Give the extent of all white blood cells.
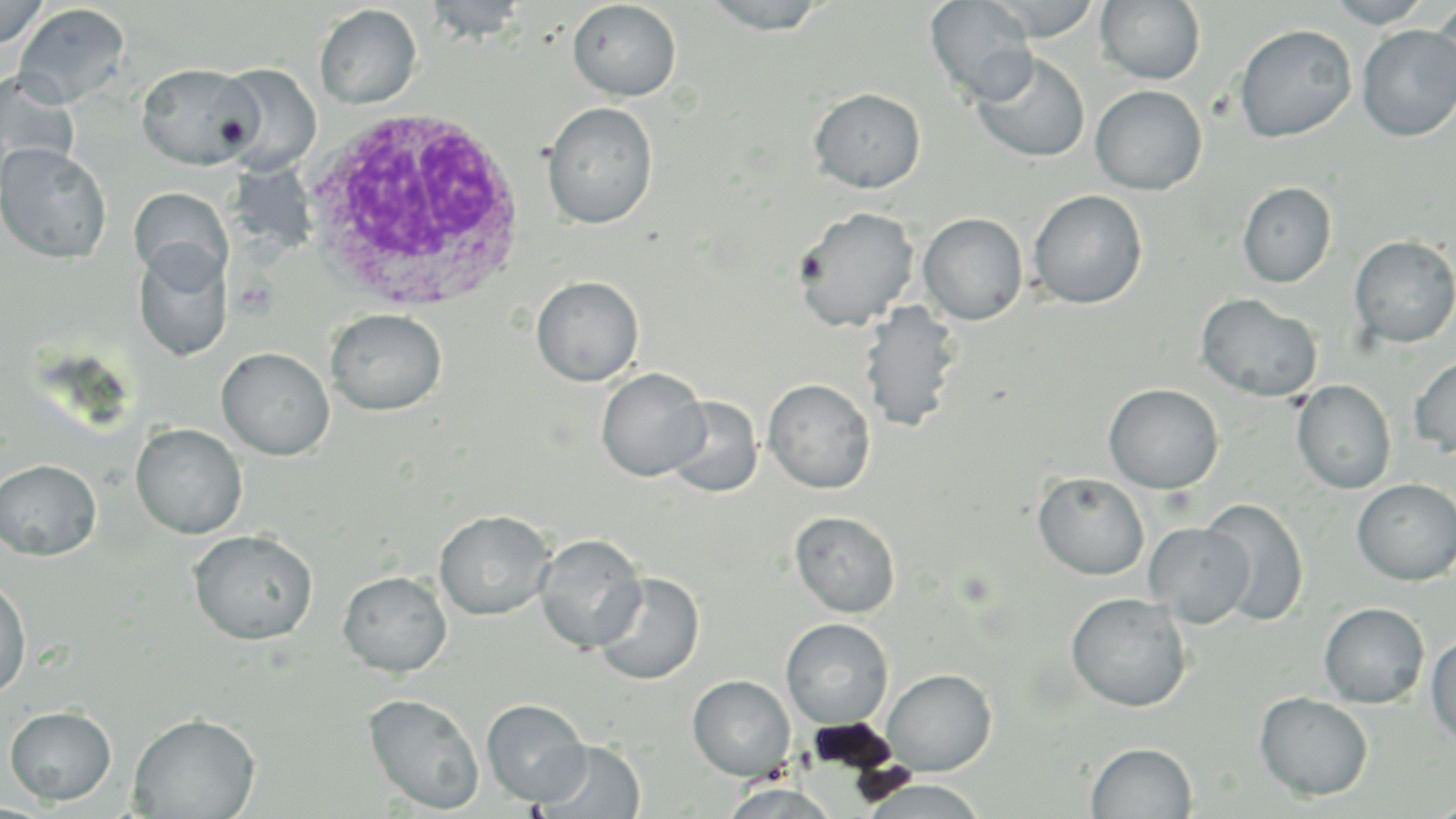

Approximate bounding boxes as (x1,y1)-(x2,y2) corner pairs in pixels.
White blood cells: (303,109)-(529,314).

Uninfected red blood cell locations: (0,0)-(50,50), (422,0)-(532,42), (696,0)-(838,33), (925,0)-(1038,104), (982,0)-(1102,41), (1095,0)-(1206,85), (1323,0)-(1435,27), (567,1)-(682,102), (1429,1)-(1456,106), (13,3)-(131,109), (315,4)-(422,109), (1234,24)-(1357,143), (1357,25)-(1456,141), (972,52)-(1090,163), (137,62)-(259,169), (214,63)-(321,175), (0,71)-(81,183), (1090,85)-(1207,195), (809,88)-(926,193), (542,102)-(658,229), (0,143)-(112,264), (1238,182)-(1337,288), (129,187)-(233,288), (1028,189)-(1148,309), (792,206)-(920,332), (918,213)-(1028,324), (1349,235)-(1456,349), (133,243)-(232,363), (531,276)-(644,386), (1196,294)-(1322,401), (859,301)-(963,432), (326,309)-(447,415), (217,348)-(335,460), (1409,355)-(1456,458), (596,367)-(709,481), (762,378)-(876,494), (1292,380)-(1396,494), (1103,383)-(1224,494), (665,396)-(763,498), (131,423)-(247,539), (0,459)-(102,560), (1033,472)-(1150,580), (1353,479)-(1456,585), (1200,498)-(1309,627), (435,510)-(555,620), (789,511)-(901,618), (1144,522)-(1254,627), (189,529)-(318,645), (535,534)-(647,653), (338,571)-(452,677), (593,572)-(705,685), (0,576)-(31,698), (1066,592)-(1192,712), (1319,602)-(1429,708), (781,618)-(893,729), (1426,631)-(1456,743), (882,669)-(996,775), (688,675)-(795,780), (1255,692)-(1374,801), (364,693)-(485,815), (481,699)-(590,805), (5,706)-(116,805), (129,713)-(260,819), (536,739)-(645,819), (1087,742)-(1197,819), (861,779)-(990,818), (720,783)-(841,819). Slide-level diagnosis: Plasmodium ovale. Thin blood film. Image is 1456×819 pixels. 1000x magnification. Single field of view. Light microscopy. May-Grünwald-Giemsa-stained preparation.